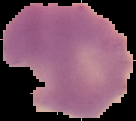

Segmented cell region on a black background. Result: malaria parasites identified. Image is 136×121 pixels. From a thin blood film.